State which parasite is depicted.
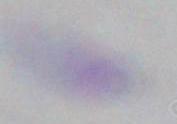

This is Toxoplasma gondii.

Captured at 1000x magnification. Micrograph.